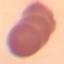
result: no malaria parasites seen
image_type: automatically extracted cell patch, resized to 64 × 64 pixels
capture: smartphone camera at the microscope eyepiece
preparation: thin blood film
stain: Giemsa